Locate every blood parasite and identify its species.
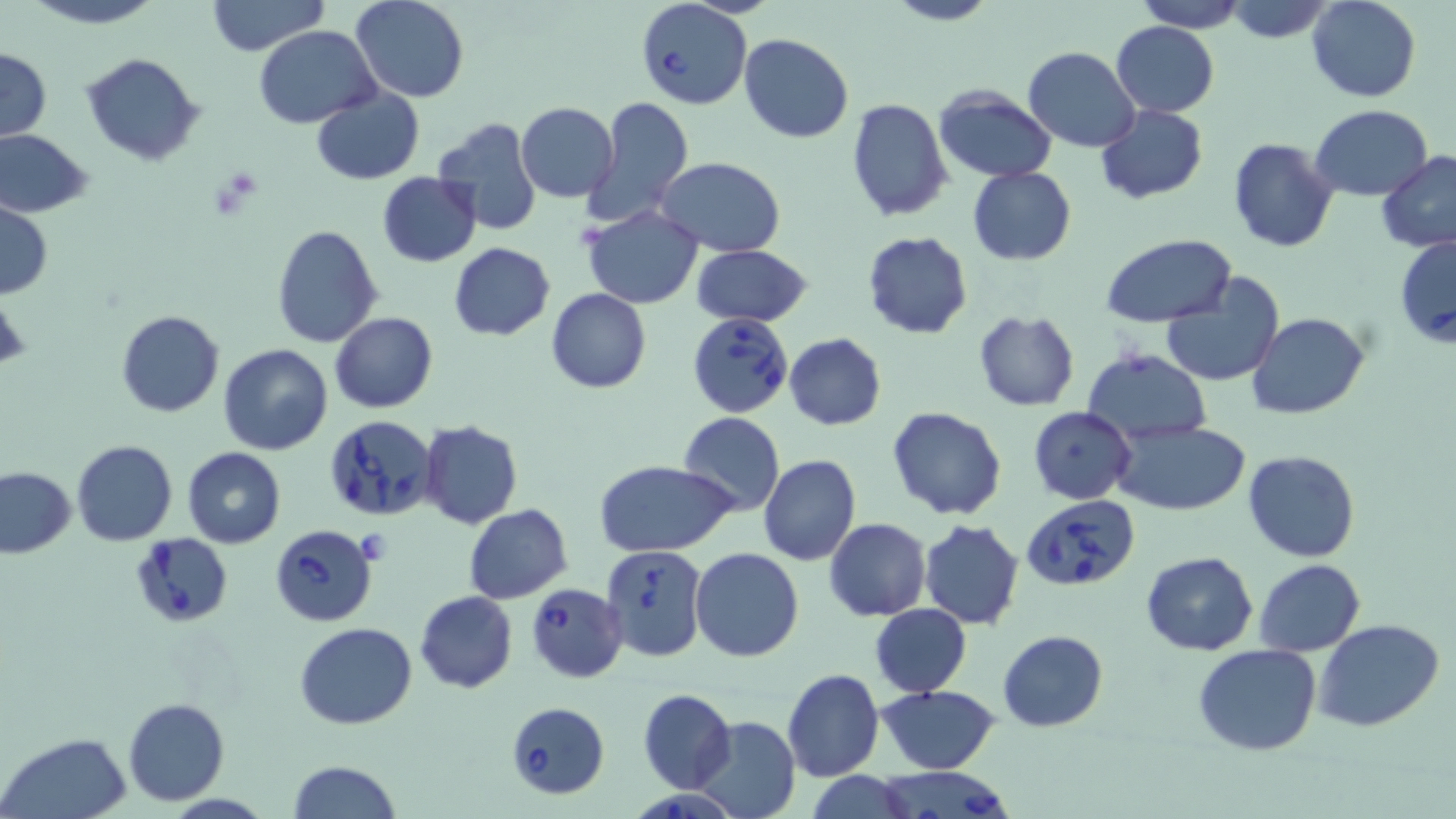

Approximate bounding boxes as (x1, y1, x2, y2) in pixels.
Babesia divergens-infected red blood cells: (634, 0, 753, 110), (1395, 235, 1456, 346), (689, 311, 792, 418), (324, 418, 436, 521), (1022, 496, 1140, 591), (269, 524, 378, 627), (137, 533, 233, 627), (600, 545, 707, 662), (526, 583, 627, 681), (505, 701, 612, 801), (872, 767, 1019, 819), (634, 790, 732, 819).
No Plasmodium falciparum, Plasmodium ovale, Plasmodium malariae, Plasmodium vivax, or Trypanosoma brucei observed.

slide_level_diagnosis: Babesia divergens
preparation: thin blood smear
uninfected_red_blood_cell_locations: 'approximate bounding boxes as (x1, y1, x2, y2) in pixels: (22, 0, 167, 28), (206, 0, 327, 55), (350, 0, 471, 103), (882, 0, 1000, 27), (1134, 0, 1246, 32), (1307, 0, 1422, 103), (1225, 1, 1337, 44), (1112, 21, 1219, 117), (254, 26, 380, 127), (738, 33, 853, 142), (1024, 46, 1140, 152), (0, 48, 51, 140), (82, 53, 203, 167), (312, 87, 424, 184), (933, 88, 1056, 181), (584, 95, 694, 228), (846, 98, 953, 222), (515, 101, 619, 201), (1095, 104, 1208, 204), (1311, 105, 1432, 200), (431, 119, 543, 237), (0, 128, 93, 218), (1229, 139, 1340, 254), (1376, 149, 1456, 253), (655, 157, 787, 255), (968, 167, 1076, 265), (376, 171, 483, 267), (0, 202, 52, 298), (583, 206, 702, 309), (272, 224, 382, 347), (862, 231, 972, 338), (1099, 233, 1237, 327), (449, 242, 554, 340), (690, 243, 813, 329), (1160, 276, 1285, 388), (546, 288, 651, 394), (1, 292, 30, 374), (115, 309, 224, 418), (973, 311, 1080, 411), (329, 313, 437, 412), (1248, 313, 1367, 420), (784, 332, 887, 431), (218, 343, 334, 456), (1082, 348, 1210, 444), (887, 405, 1007, 521), (1027, 407, 1135, 505), (679, 412, 784, 517), (1111, 420, 1251, 514), (420, 421, 523, 530), (71, 439, 177, 546), (182, 446, 286, 548), (1243, 449, 1362, 563), (759, 453, 861, 566), (595, 460, 738, 558), (0, 467, 75, 557), (464, 504, 572, 603), (824, 518, 931, 620), (919, 519, 1024, 630), (690, 547, 804, 663), (1140, 552, 1257, 656), (1255, 558, 1365, 656), (414, 591, 518, 694), (870, 604, 971, 696), (1315, 620, 1444, 732), (295, 621, 417, 729), (999, 631, 1108, 731), (1193, 644, 1322, 756), (781, 668, 884, 782), (877, 685, 1000, 774), (637, 688, 737, 794), (123, 698, 231, 804), (691, 715, 799, 819), (0, 733, 132, 819), (286, 759, 400, 819), (805, 772, 919, 818)'
stain: May-Grünwald-Giemsa
modality: optical microscopy
magnification: 1000x
field_of_view: one of a larger specimen
image_size: 1456×819 pixels